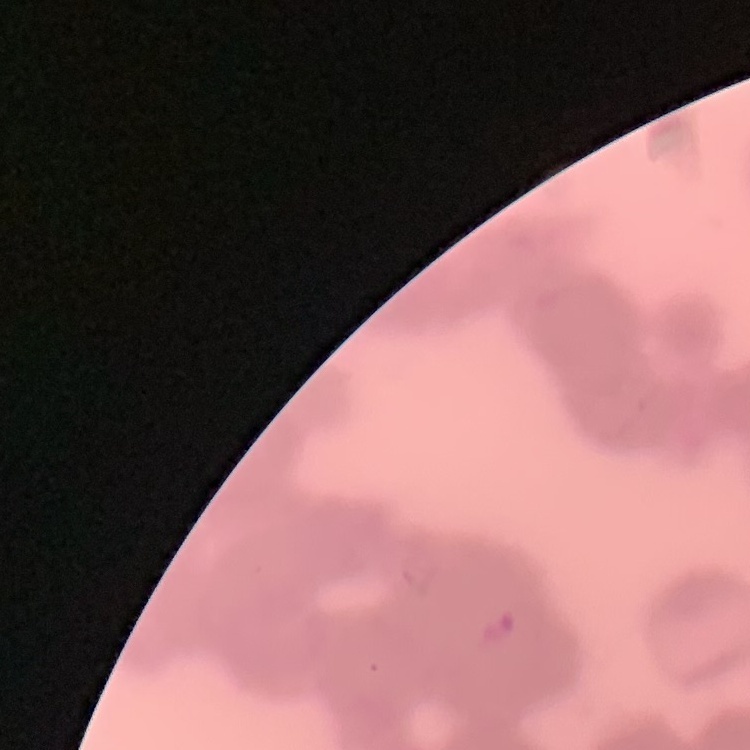

The red blood cells show rouleaux formation. Thin blood film. Stained with either Field's or Giemsa. Square crop of a larger photomicrograph.